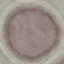
Summary:
  - Result: no malaria parasites detected
  - Capture: smartphone camera at the microscope eyepiece
  - Preparation: thin blood film
  - Stain: Giemsa
  - Image type: cell patch, automatically extracted from a larger field of view and resized to 64 × 64 pixels